Locate every Plasmodium falciparum-infected red blood cell.
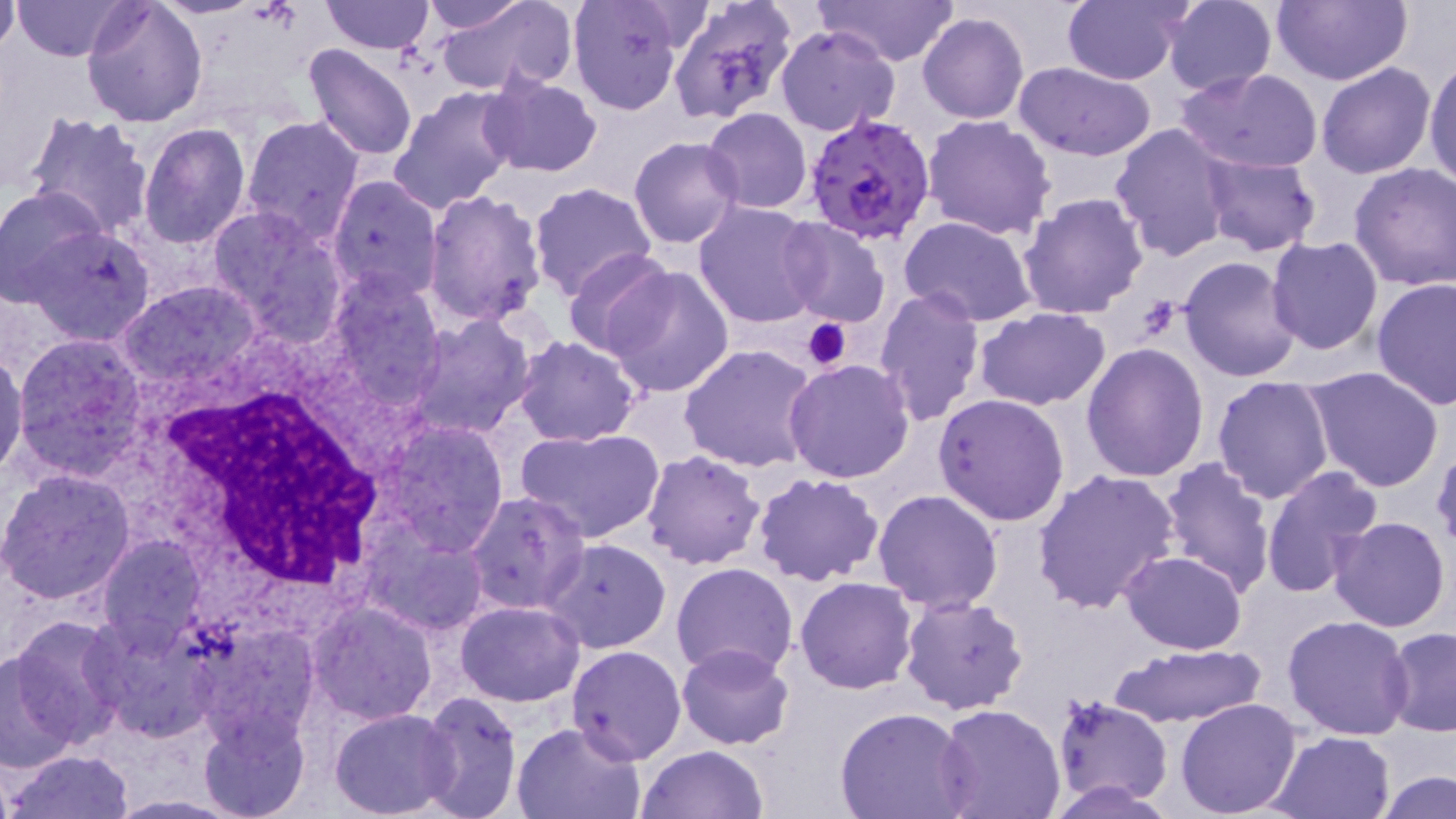
Approximate bounding boxes as named x1/y1/x2/y2 corners in pixels.
Plasmodium falciparum-infected red blood cells: (x1=803, y1=112, x2=938, y2=247).

slide-level diagnosis = Plasmodium falciparum
preparation = thin blood film
image size = 1456×819 pixels
uninfected red blood cell locations = approximate bounding boxes as named x1/y1/x2/y2 corners in pixels: (x1=11, y1=0, x2=136, y2=61), (x1=150, y1=0, x2=262, y2=21), (x1=319, y1=0, x2=433, y2=54), (x1=417, y1=0, x2=530, y2=35), (x1=432, y1=0, x2=576, y2=97), (x1=818, y1=0, x2=963, y2=66), (x1=1062, y1=0, x2=1192, y2=86), (x1=1162, y1=0, x2=1277, y2=94), (x1=1271, y1=0, x2=1410, y2=86), (x1=80, y1=1, x2=209, y2=128), (x1=568, y1=1, x2=686, y2=114), (x1=667, y1=1, x2=797, y2=122), (x1=0, y1=4, x2=19, y2=53), (x1=455, y1=8, x2=590, y2=170), (x1=918, y1=13, x2=1029, y2=125), (x1=775, y1=25, x2=901, y2=135), (x1=302, y1=45, x2=419, y2=164), (x1=1424, y1=52, x2=1456, y2=191), (x1=1012, y1=61, x2=1157, y2=162), (x1=1316, y1=63, x2=1436, y2=181), (x1=1175, y1=67, x2=1323, y2=174), (x1=478, y1=75, x2=601, y2=177), (x1=387, y1=88, x2=521, y2=214), (x1=703, y1=108, x2=812, y2=214), (x1=24, y1=110, x2=156, y2=239), (x1=922, y1=115, x2=1056, y2=242), (x1=239, y1=116, x2=366, y2=247), (x1=137, y1=123, x2=252, y2=249), (x1=1109, y1=123, x2=1237, y2=263), (x1=629, y1=137, x2=743, y2=250), (x1=1200, y1=152, x2=1323, y2=257), (x1=1349, y1=163, x2=1456, y2=291), (x1=324, y1=175, x2=443, y2=304), (x1=528, y1=180, x2=657, y2=302), (x1=0, y1=184, x2=107, y2=308), (x1=422, y1=190, x2=547, y2=327), (x1=1017, y1=192, x2=1150, y2=319), (x1=693, y1=199, x2=821, y2=330), (x1=205, y1=204, x2=349, y2=346), (x1=901, y1=217, x2=1038, y2=326), (x1=778, y1=220, x2=890, y2=328), (x1=21, y1=225, x2=156, y2=345), (x1=1266, y1=237, x2=1383, y2=355), (x1=564, y1=250, x2=678, y2=355), (x1=1178, y1=255, x2=1303, y2=382), (x1=598, y1=264, x2=736, y2=396), (x1=325, y1=271, x2=447, y2=409), (x1=1371, y1=278, x2=1456, y2=410), (x1=118, y1=281, x2=262, y2=389), (x1=872, y1=287, x2=987, y2=424), (x1=974, y1=307, x2=1112, y2=411), (x1=402, y1=314, x2=538, y2=441), (x1=12, y1=333, x2=148, y2=475), (x1=513, y1=335, x2=642, y2=446), (x1=1081, y1=343, x2=1208, y2=482), (x1=679, y1=344, x2=820, y2=473), (x1=0, y1=350, x2=27, y2=479), (x1=784, y1=359, x2=915, y2=484), (x1=1305, y1=368, x2=1445, y2=494), (x1=1211, y1=375, x2=1334, y2=505), (x1=934, y1=394, x2=1071, y2=526), (x1=378, y1=420, x2=510, y2=557), (x1=516, y1=427, x2=668, y2=544), (x1=642, y1=451, x2=765, y2=569), (x1=1156, y1=457, x2=1275, y2=598), (x1=1260, y1=465, x2=1383, y2=597), (x1=0, y1=468, x2=137, y2=605), (x1=1034, y1=468, x2=1178, y2=615), (x1=752, y1=471, x2=884, y2=588), (x1=872, y1=488, x2=1003, y2=613), (x1=464, y1=492, x2=590, y2=614), (x1=1328, y1=515, x2=1451, y2=633), (x1=362, y1=528, x2=488, y2=636), (x1=97, y1=534, x2=208, y2=649), (x1=542, y1=538, x2=671, y2=653), (x1=1121, y1=551, x2=1248, y2=654), (x1=669, y1=561, x2=798, y2=678), (x1=795, y1=576, x2=919, y2=693), (x1=899, y1=593, x2=1030, y2=715), (x1=308, y1=599, x2=438, y2=723), (x1=456, y1=600, x2=585, y2=706), (x1=85, y1=614, x2=219, y2=741), (x1=1282, y1=614, x2=1415, y2=741), (x1=5, y1=616, x2=130, y2=751), (x1=190, y1=616, x2=323, y2=743), (x1=1382, y1=627, x2=1456, y2=739), (x1=1110, y1=642, x2=1265, y2=727), (x1=567, y1=645, x2=687, y2=766), (x1=676, y1=645, x2=795, y2=749), (x1=0, y1=655, x2=79, y2=772), (x1=415, y1=691, x2=525, y2=819), (x1=1051, y1=695, x2=1173, y2=806), (x1=1175, y1=696, x2=1303, y2=818), (x1=935, y1=705, x2=1067, y2=819), (x1=196, y1=707, x2=311, y2=819), (x1=330, y1=708, x2=457, y2=817), (x1=834, y1=708, x2=973, y2=818), (x1=511, y1=721, x2=645, y2=819), (x1=1269, y1=730, x2=1394, y2=817), (x1=635, y1=745, x2=769, y2=819), (x1=8, y1=749, x2=132, y2=819), (x1=1375, y1=769, x2=1456, y2=819), (x1=1039, y1=779, x2=1183, y2=817), (x1=105, y1=794, x2=242, y2=817)
platelet locations = approximate bounding boxes as named x1/y1/x2/y2 corners in pixels: (x1=799, y1=317, x2=852, y2=372)
stain = May-Grünwald-Giemsa
modality = light microscopy
white blood cell locations = approximate bounding boxes as named x1/y1/x2/y2 corners in pixels: (x1=149, y1=356, x2=401, y2=613)
field of view = one of a larger specimen
magnification = 1000x